Name the cell type shown.
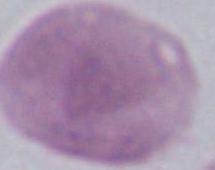
An erythrocyte.

Summary:
  - Magnification: 1000x
  - Modality: micrograph